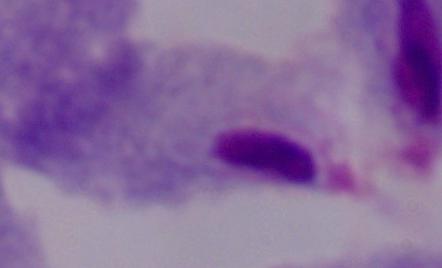

Summary:
  - Magnification: 1000x
  - Modality: photomicrograph
  - Identification: trichomonad